Identify the blood parasite species.
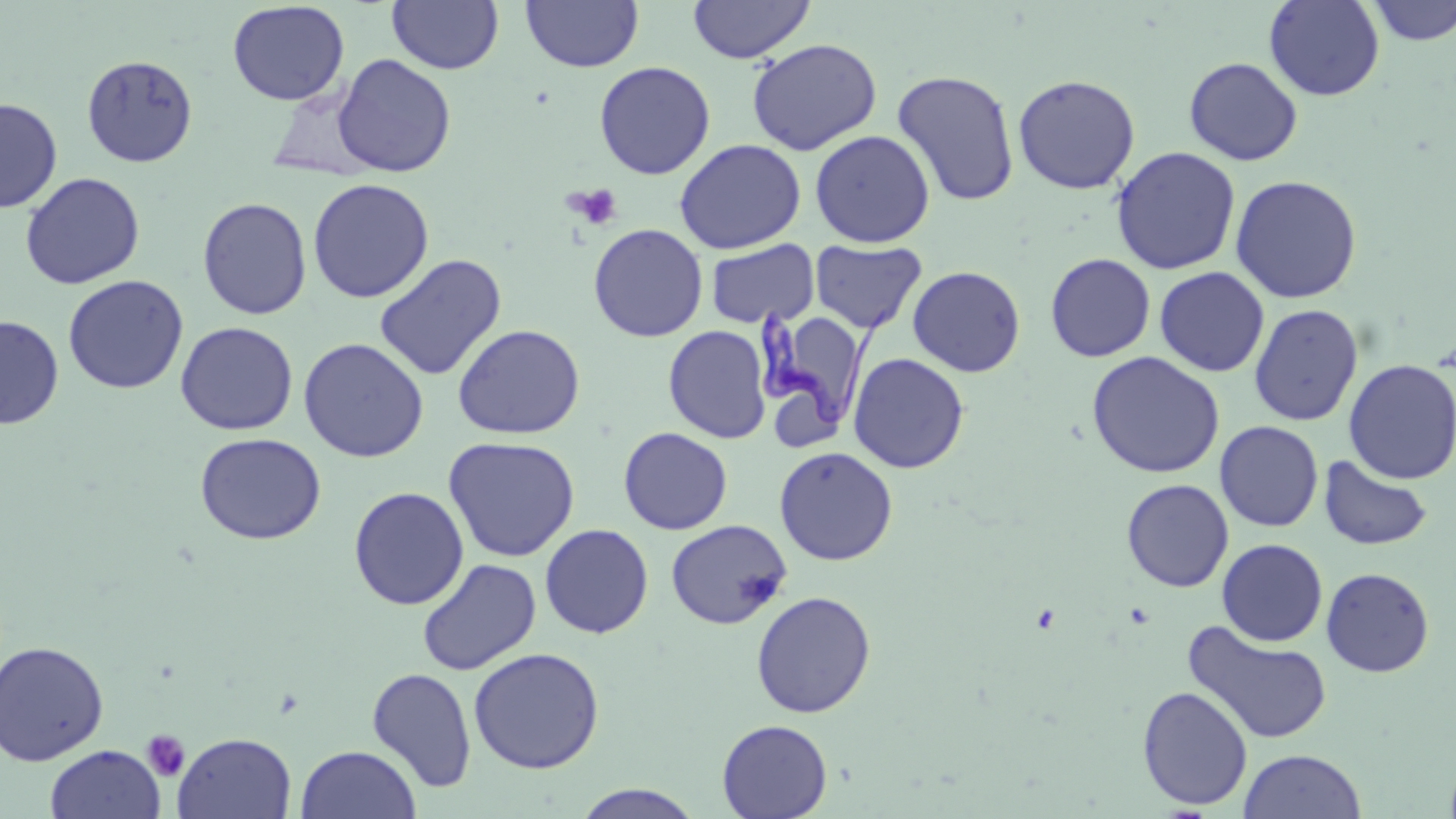

Trypanosoma brucei.

preparation = thin blood smear
field of view = single
modality = light microscopy
image size = 1456×819 pixels
stain = May-Grünwald-Giemsa
magnification = 1000x
platelet locations = approximate bounding boxes as (x1, y1, x2, y2) in pixels: (566, 184, 622, 230), (142, 729, 190, 781)
uninfected red blood cell locations = approximate bounding boxes as (x1, y1, x2, y2) in pixels: (387, 0, 504, 75), (521, 0, 643, 72), (687, 0, 815, 64), (1264, 0, 1385, 101), (1363, 0, 1456, 46), (227, 2, 350, 106), (747, 38, 882, 155), (81, 54, 198, 168), (332, 54, 457, 177), (1183, 57, 1303, 166), (594, 60, 715, 180), (891, 69, 1020, 206), (1012, 74, 1140, 195), (0, 97, 62, 213), (810, 130, 935, 248), (674, 138, 806, 255), (1111, 146, 1241, 275), (20, 172, 145, 290), (1229, 174, 1362, 304), (307, 178, 434, 304), (197, 197, 312, 320), (588, 224, 708, 342), (706, 239, 820, 328), (810, 240, 926, 334), (1045, 253, 1156, 362), (374, 254, 506, 381), (907, 265, 1026, 377), (1154, 266, 1269, 377), (61, 275, 189, 395), (1249, 304, 1363, 426), (0, 315, 64, 429), (779, 319, 856, 443), (175, 321, 298, 435), (452, 323, 585, 440), (663, 325, 772, 444), (298, 337, 429, 463), (1086, 351, 1225, 479), (847, 352, 969, 473), (1343, 359, 1456, 484), (1215, 421, 1324, 532), (618, 426, 733, 535), (195, 433, 326, 545), (442, 436, 581, 562), (774, 446, 898, 565), (1318, 455, 1434, 551), (1121, 478, 1234, 592), (348, 486, 469, 610), (665, 519, 792, 629), (540, 523, 654, 638), (1217, 538, 1328, 647), (416, 558, 542, 675), (1321, 567, 1434, 677), (750, 590, 876, 718), (1182, 620, 1333, 745), (0, 640, 109, 766), (468, 646, 605, 774), (367, 667, 477, 792), (1137, 685, 1253, 811), (717, 719, 833, 819), (173, 732, 296, 818), (45, 744, 165, 819), (295, 744, 422, 819), (1443, 747, 1456, 819), (1238, 749, 1367, 819), (571, 784, 705, 818)
Trypanosoma brucei locations = approximate bounding boxes as (x1, y1, x2, y2) in pixels: (754, 301, 900, 430)